Locate and identify every blood parasite.
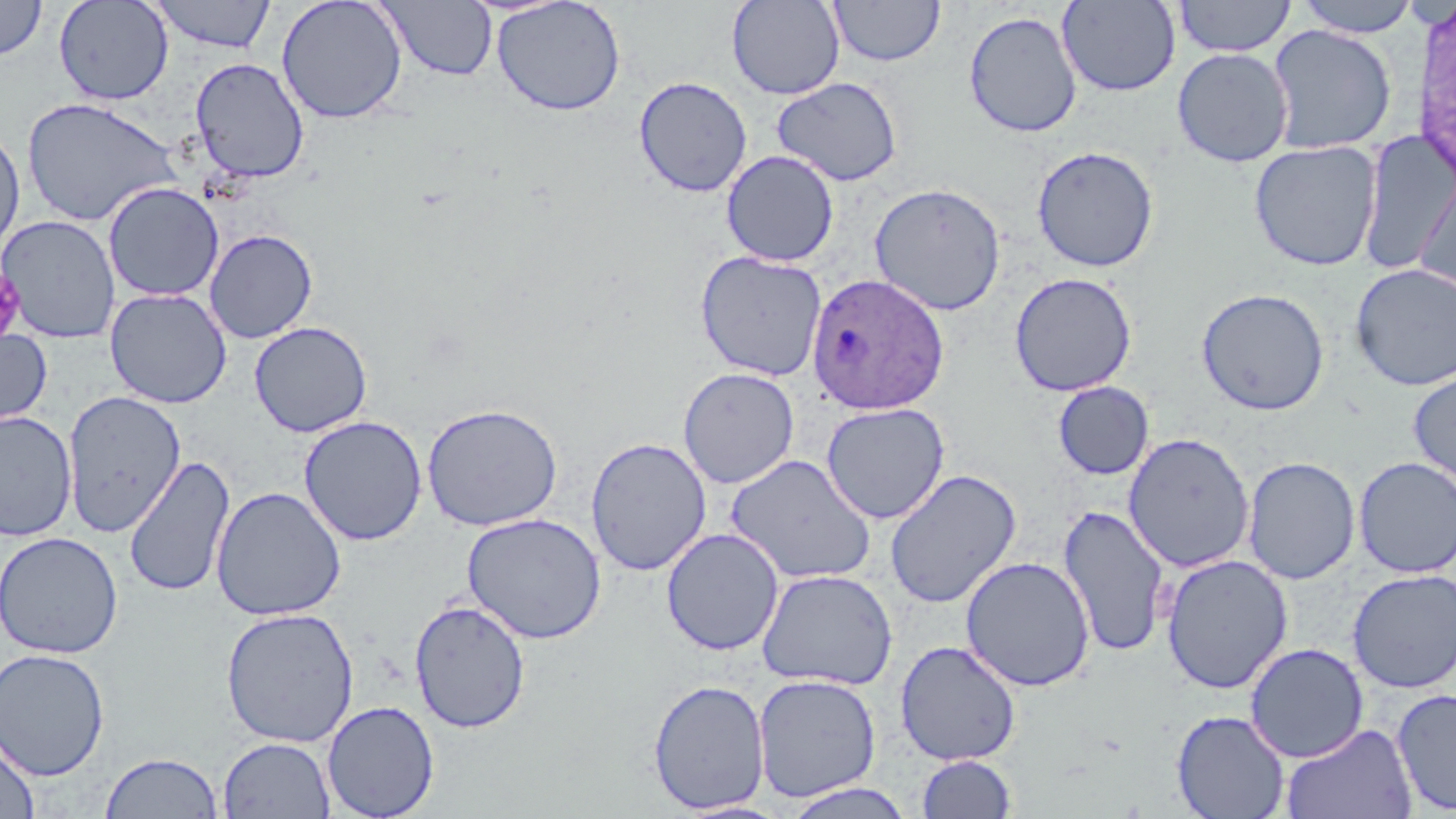
Approximate bounding boxes as [x1, y1, x2, y2] in pixels.
Plasmodium ovale-infected red blood cells (subset): [806, 272, 950, 415].
No Plasmodium falciparum, Plasmodium malariae, Plasmodium vivax, Babesia divergens, or Trypanosoma brucei observed.

Summary:
  - Uninfected red blood cell locations (subset): [0, 0, 47, 61], [53, 0, 174, 105], [149, 0, 277, 53], [276, 0, 408, 124], [491, 0, 626, 116], [727, 0, 846, 100], [829, 0, 946, 67], [1173, 0, 1296, 57], [1294, 0, 1422, 37], [377, 1, 498, 82], [1056, 1, 1181, 96], [964, 10, 1082, 139], [1267, 24, 1396, 154], [1172, 47, 1294, 167], [190, 56, 309, 182], [634, 75, 752, 197], [771, 77, 903, 187], [21, 96, 182, 228], [0, 123, 25, 260], [1357, 131, 1454, 275], [1249, 140, 1383, 271], [1031, 145, 1159, 272], [721, 149, 839, 267], [1415, 167, 1456, 296], [102, 182, 224, 302], [0, 215, 121, 343], [204, 229, 318, 343], [695, 250, 827, 381], [1350, 263, 1456, 391], [1009, 272, 1137, 396], [105, 288, 231, 408], [1196, 288, 1329, 416], [249, 321, 373, 437], [0, 327, 53, 433], [678, 367, 799, 488], [1408, 368, 1456, 492], [1053, 381, 1154, 480], [61, 390, 186, 537], [421, 402, 563, 531], [821, 402, 950, 524], [0, 411, 77, 542], [298, 415, 428, 546], [1123, 432, 1255, 573], [586, 436, 712, 576], [724, 453, 876, 584], [124, 454, 236, 599], [1243, 456, 1361, 584], [1353, 457, 1456, 578], [884, 468, 1021, 609], [210, 486, 347, 621], [1058, 503, 1170, 658], [462, 512, 607, 644], [661, 528, 784, 656], [0, 531, 123, 658], [1161, 553, 1293, 694], [961, 556, 1095, 692], [756, 569, 897, 690], [1347, 569, 1456, 694], [409, 599, 531, 734], [220, 607, 359, 747], [894, 640, 1021, 765], [1245, 642, 1369, 763], [0, 648, 110, 781], [752, 674, 882, 802], [647, 679, 771, 814], [1392, 687, 1456, 815], [321, 700, 440, 818], [1172, 709, 1290, 819], [1282, 723, 1418, 819], [0, 731, 39, 818], [218, 737, 335, 819], [100, 751, 224, 818], [916, 754, 1017, 818], [780, 783, 916, 818]
  - Platelet locations: [0, 266, 26, 344]
  - Slide-level diagnosis: Plasmodium ovale
  - Preparation: thin blood smear
  - Stain: May-Grünwald-Giemsa
  - Image size: 1456×819 pixels
  - Magnification: 1000x
  - Modality: optical microscopy
  - Field of view: single